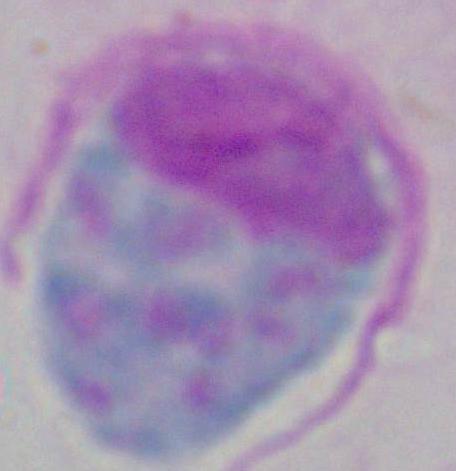

modality = photomicrograph
identification = white blood cell
magnification = 1000x